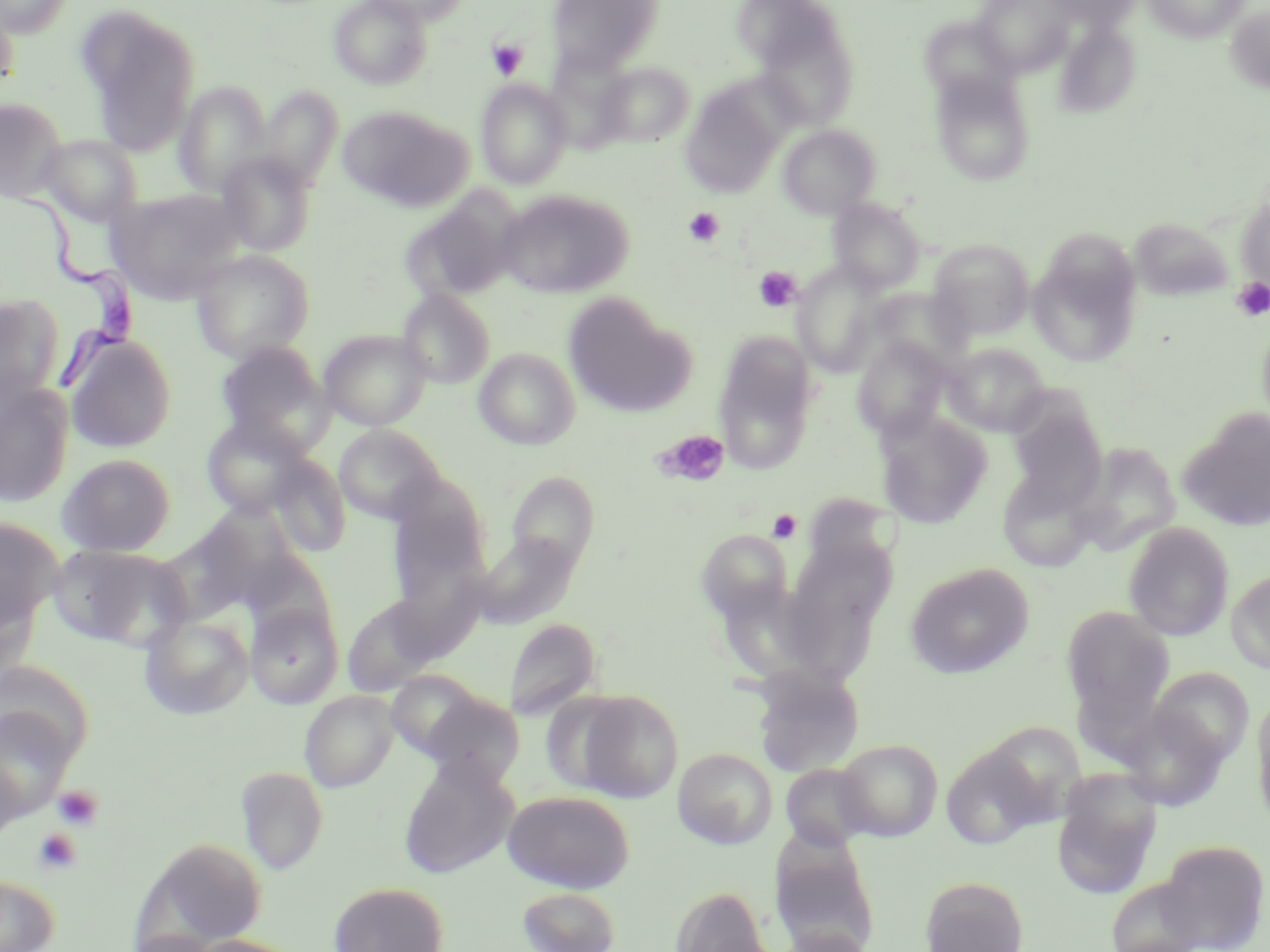

Approximate bounding boxes as (x1, y1, x2, y2) in pixels. Trypanosoma brucei locations: (20, 189, 142, 396). Platelet locations: (486, 38, 529, 80), (683, 207, 724, 247), (754, 266, 802, 312), (1231, 279, 1270, 321), (655, 429, 730, 486), (767, 509, 802, 543), (53, 785, 104, 831), (33, 828, 82, 874). Uninfected red blood cell locations: (0, 0, 74, 38), (329, 0, 433, 90), (357, 0, 474, 25), (546, 0, 665, 78), (972, 0, 1076, 78), (1044, 0, 1142, 31), (1144, 0, 1249, 43), (0, 5, 21, 91), (1224, 5, 1270, 93), (77, 8, 200, 153), (919, 14, 1018, 105), (755, 16, 860, 132), (1054, 20, 1141, 119), (595, 61, 694, 146), (929, 70, 1036, 186), (475, 79, 573, 189), (175, 81, 272, 196), (679, 84, 786, 199), (257, 86, 344, 190), (0, 97, 68, 204), (338, 105, 473, 212), (778, 124, 880, 219), (40, 134, 143, 227), (216, 152, 317, 256), (109, 189, 243, 303), (496, 189, 633, 298), (403, 194, 521, 302), (1235, 194, 1270, 291), (828, 198, 925, 292), (1129, 217, 1233, 301), (929, 239, 1035, 340), (1029, 246, 1141, 367), (191, 250, 314, 362), (791, 261, 887, 377), (397, 289, 495, 389), (0, 294, 65, 407), (563, 294, 694, 418), (1256, 312, 1270, 435), (318, 329, 432, 430), (65, 335, 177, 453), (713, 335, 819, 474), (851, 337, 952, 440), (214, 341, 330, 449), (943, 342, 1050, 437), (474, 348, 581, 450), (0, 383, 74, 507), (1007, 403, 1108, 510), (1179, 411, 1270, 531), (875, 412, 992, 528), (201, 416, 315, 518), (334, 424, 445, 523), (1071, 443, 1182, 556), (57, 453, 176, 556), (266, 454, 351, 557), (506, 472, 600, 573), (388, 473, 492, 577), (153, 513, 280, 624), (0, 517, 64, 631), (1123, 522, 1234, 641), (696, 529, 792, 621), (473, 533, 580, 629), (50, 544, 189, 650), (241, 550, 337, 640), (904, 563, 1036, 679), (1225, 568, 1270, 673), (342, 595, 440, 696), (245, 603, 343, 708), (1061, 606, 1174, 725), (139, 614, 253, 719), (504, 618, 602, 720), (0, 665, 94, 769), (751, 667, 864, 778), (1149, 667, 1253, 768), (386, 670, 485, 760), (300, 690, 398, 792), (572, 690, 684, 802), (422, 691, 525, 787), (1251, 692, 1270, 831), (1117, 703, 1230, 812), (0, 706, 77, 820), (977, 721, 1087, 825), (835, 739, 943, 841), (940, 742, 1048, 850), (673, 748, 778, 849), (0, 756, 22, 843), (398, 757, 519, 879), (781, 763, 874, 851), (236, 766, 328, 873), (1051, 770, 1163, 898), (502, 790, 635, 893), (141, 836, 268, 948), (1158, 839, 1269, 951), (772, 848, 880, 951), (0, 874, 60, 952), (920, 875, 1029, 952), (1105, 876, 1207, 952), (328, 881, 449, 952), (516, 885, 621, 952), (670, 885, 772, 951), (776, 928, 876, 952), (181, 934, 307, 952). Slide-level diagnosis: Trypanosoma brucei. Image is 1270×952 pixels. Light microscopy. May-Grünwald-Giemsa-stained preparation. Thin blood film. Single field of view. 1000x magnification.